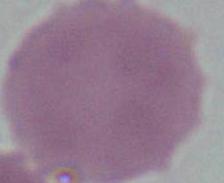
Summary:
  - Magnification: 1000x
  - Identification: erythrocyte
  - Modality: photomicrograph